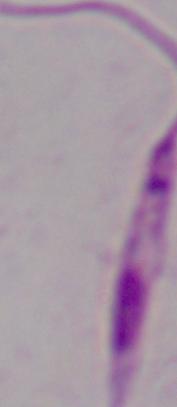

Summary:
  - Magnification: 1000x
  - Identification: Leishmania
  - Modality: photomicrograph